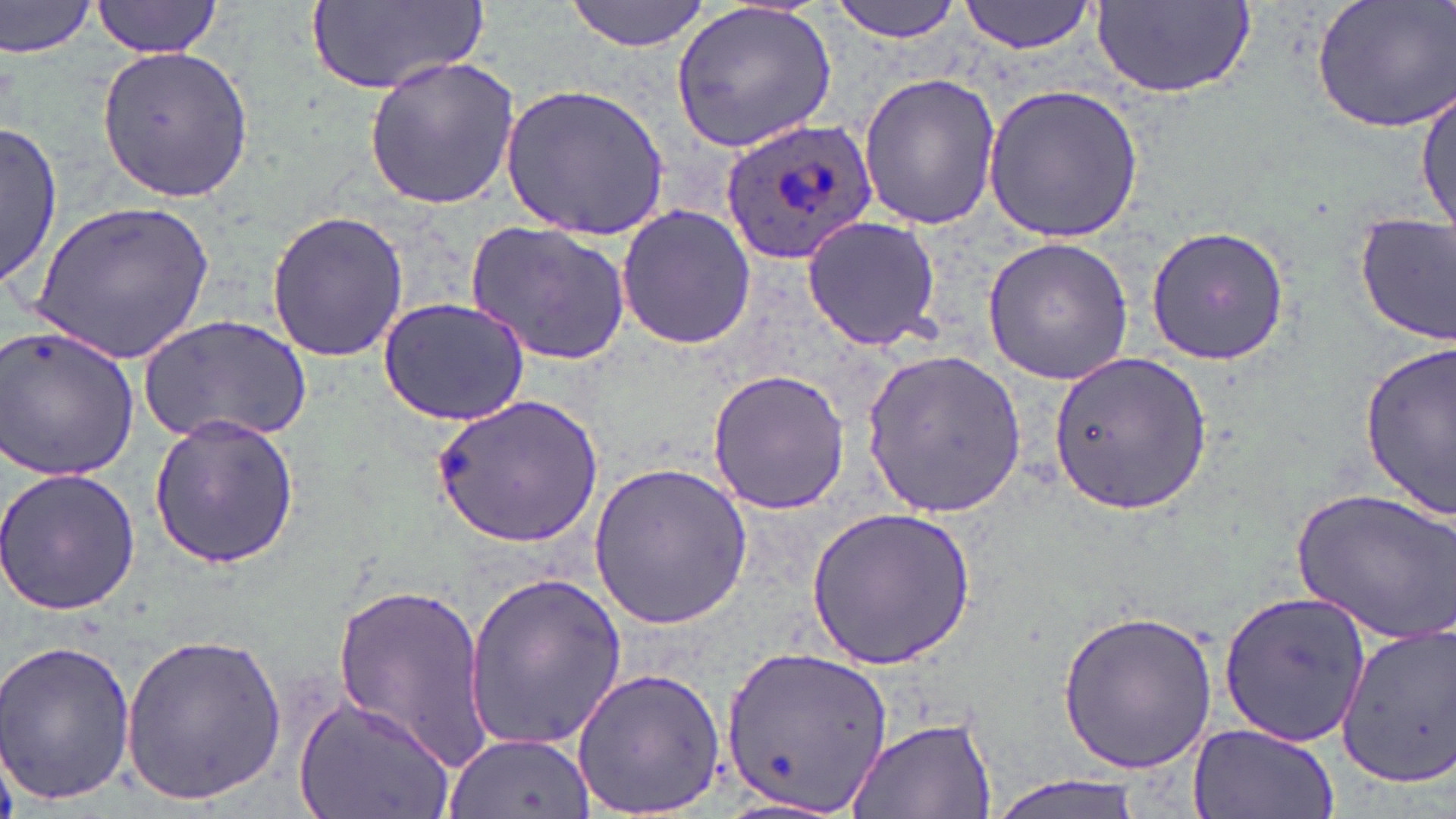
Summary:
  - Coordinate format: approximate bounding boxes as (x1, y1, x2, y2) in pixels
  - Uninfected red blood cell locations: (304, 0, 485, 98), (566, 0, 709, 52), (828, 0, 963, 42), (958, 0, 1102, 55), (1310, 0, 1456, 135), (1, 1, 103, 59), (92, 1, 224, 57), (667, 1, 841, 155), (1093, 2, 1255, 101), (97, 44, 252, 203), (364, 56, 520, 209), (858, 73, 1001, 230), (982, 82, 1143, 243), (501, 84, 670, 239), (1415, 87, 1454, 237), (0, 121, 62, 289), (32, 198, 217, 361), (615, 204, 757, 351), (265, 210, 409, 363), (1354, 211, 1456, 346), (800, 214, 944, 351), (468, 220, 631, 365), (1145, 222, 1291, 366), (982, 236, 1134, 385), (377, 297, 531, 425), (140, 314, 311, 447), (0, 323, 141, 481), (1358, 344, 1456, 520), (862, 348, 1027, 519), (1048, 349, 1213, 517), (706, 369, 851, 514), (434, 393, 602, 546), (149, 414, 300, 569), (588, 461, 753, 632), (0, 465, 142, 618), (1291, 486, 1456, 644), (807, 506, 974, 670), (464, 567, 629, 757), (331, 581, 490, 768), (1218, 592, 1374, 748), (1055, 607, 1221, 773), (1335, 620, 1455, 792), (120, 632, 287, 807), (0, 636, 136, 807), (719, 645, 893, 816), (569, 665, 728, 819), (296, 692, 457, 819), (844, 715, 997, 819), (1187, 722, 1340, 819), (444, 731, 595, 818), (980, 774, 1153, 819)
  - Plasmodium ovale-infected red blood cell locations: (720, 117, 875, 264)
  - Slide-level diagnosis: Plasmodium ovale
  - Modality: optical microscopy
  - Image size: 1456×819 pixels
  - Preparation: thin blood smear
  - Field of view: single
  - Magnification: 1000x
  - Stain: May-Grünwald-Giemsa